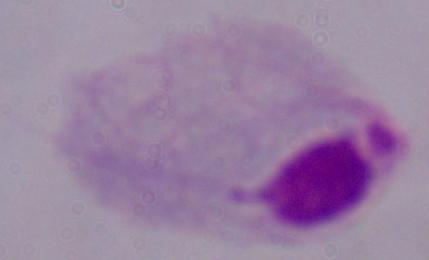
identification: trichomonad
magnification: 1000x
modality: photomicrograph